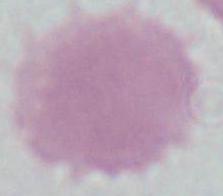
modality = micrograph
identification = red blood cell
magnification = 1000x